Identify the preparation type.
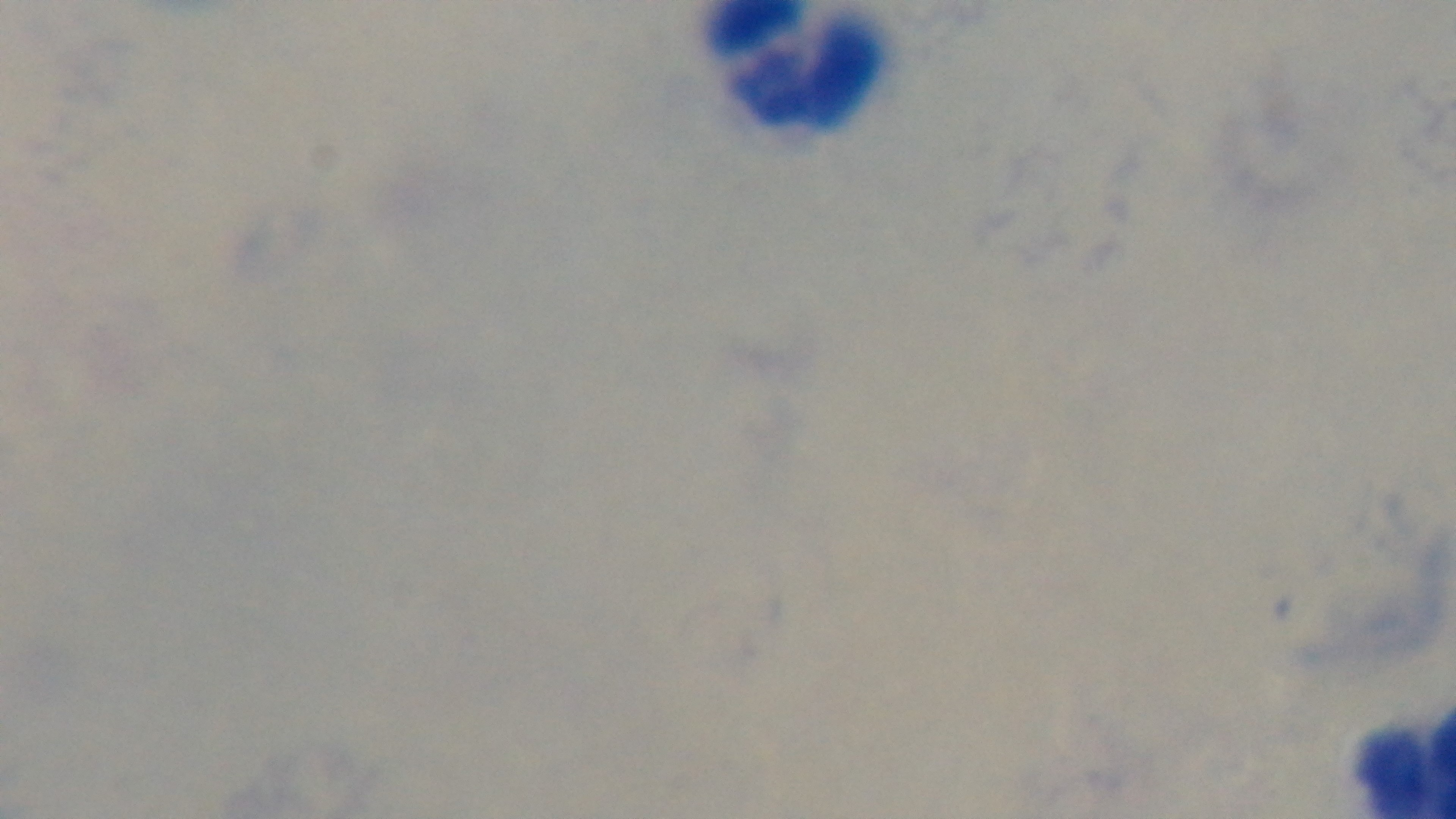
It is a thick blood film.

malaria status = uninfected
capture = mounted 4K digital camera
objective = 100x oil immersion
modality = light microscopy
field of view = single
stain = Giemsa